Point out every Plasmodium parasite and every leukocyte.
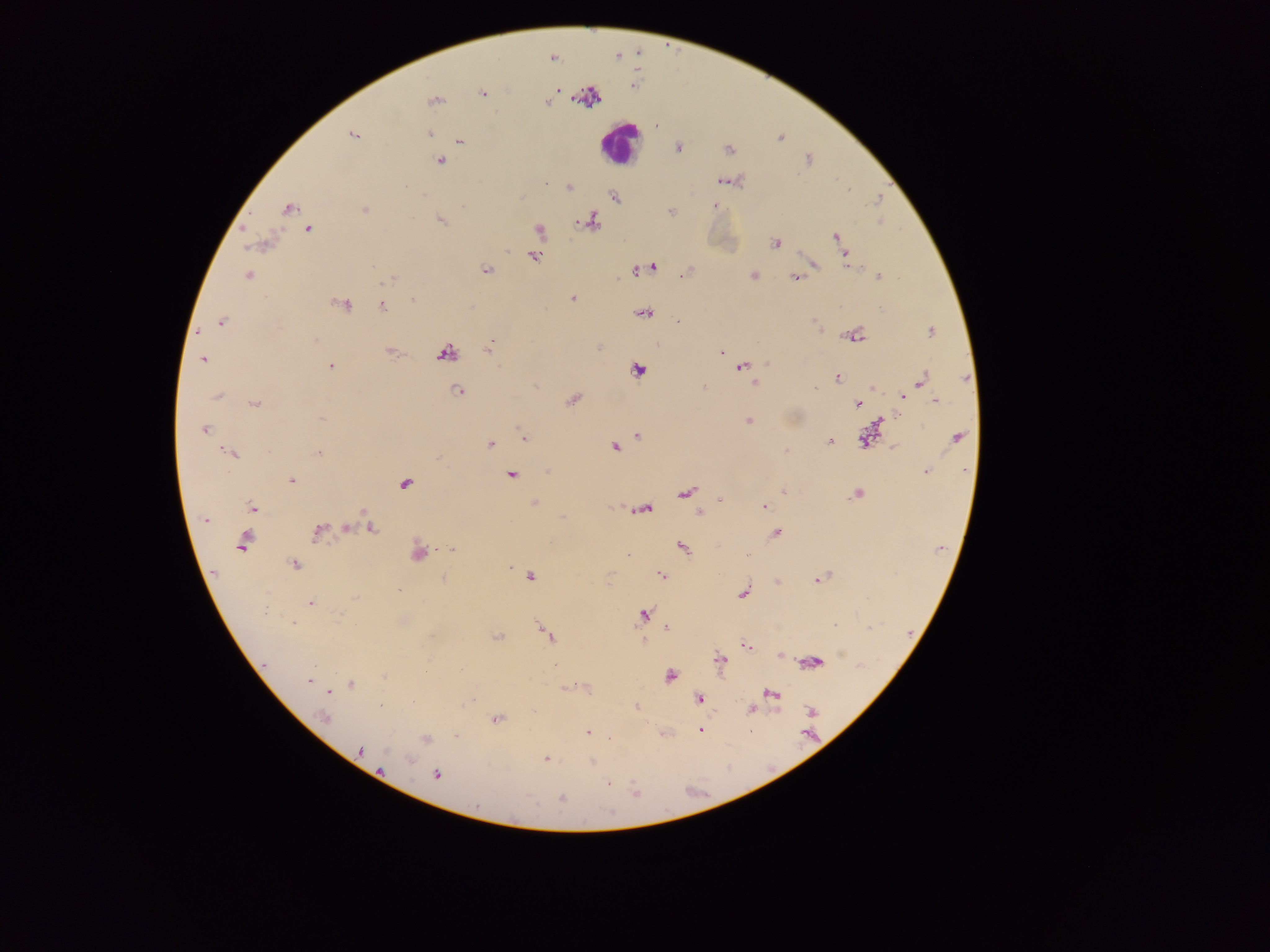

Approximate centers as {x, y} in pixels.
Plasmodium parasites: {552, 57}, {557, 88}, {482, 93}, {434, 100}, {547, 101}, {429, 133}, {352, 134}, {780, 137}, {459, 140}, {678, 147}, {727, 149}, {440, 160}, {723, 180}, {544, 183}, {568, 186}, {615, 197}, {715, 206}, {287, 208}, {365, 210}, {670, 211}, {440, 219}, {591, 221}, {309, 228}, {537, 231}, {836, 236}, {259, 243}, {774, 243}, {843, 253}, {533, 256}, {812, 263}, {652, 267}, {485, 270}, {639, 270}, {248, 274}, {684, 274}, {803, 275}, {754, 276}, {878, 276}, {796, 277}, {388, 278}, {572, 298}, {412, 299}, {342, 303}, {382, 306}, {643, 312}, {221, 321}, {677, 321}, {930, 330}, {853, 336}, {488, 350}, {391, 351}, {722, 352}, {445, 353}, {202, 359}, {742, 366}, {331, 367}, {637, 369}, {836, 376}, {921, 379}, {755, 383}, {871, 386}, {703, 387}, {458, 390}, {216, 395}, {901, 396}, {573, 399}, {935, 401}, {255, 403}, {857, 403}, {321, 418}, {748, 420}, {204, 428}, {870, 433}, {636, 434}, {524, 437}, {956, 438}, {865, 439}, {829, 440}, {489, 444}, {614, 446}, {893, 448}, {785, 450}, {231, 453}, {318, 453}, {437, 455}, {925, 471}, {511, 474}, {291, 479}, {405, 483}, {784, 491}, {684, 492}, {857, 494}, {720, 501}, {534, 503}, {763, 506}, {252, 508}, {644, 508}, {362, 511}, {699, 512}, {205, 518}, {369, 527}, {345, 528}, {317, 532}, {775, 533}, {244, 540}, {681, 547}, {451, 549}, {418, 551}, {293, 564}, {510, 565}, {530, 575}, {660, 576}, {821, 578}, {442, 579}, {777, 582}, {399, 589}, {744, 592}, {310, 603}, {265, 613}, {644, 614}, {292, 622}, {541, 627}, {666, 629}, {548, 635}, {497, 637}, {644, 641}, {745, 645}, {780, 654}, {719, 660}, {811, 662}, {670, 675}, {384, 677}, {309, 680}, {350, 684}, {564, 688}, {330, 692}, {770, 694}, {698, 698}, {380, 705}, {636, 706}, {750, 708}, {324, 717}, {496, 718}, {701, 730}, {587, 732}, {663, 733}, {425, 739}, {359, 750}, {545, 758}, {590, 761}, {436, 775}, {608, 782}.
Leukocytes: {620, 143}.

image size = 1270×952 pixels
country = Ghana
capture = mobile-phone photograph through a microscope
preparation = thick blood smear
field of view = single